Assess this cell for malaria.
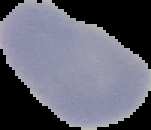
Uninfected.

image_size: 151×130 pixels
preparation: thin blood smear
image_type: segmented cell region with the area outside set to black